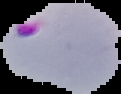
image size = 121×94 pixels
image type = segmented cell region with the area outside set to black
result = Plasmodium parasites detected
preparation = thin blood film